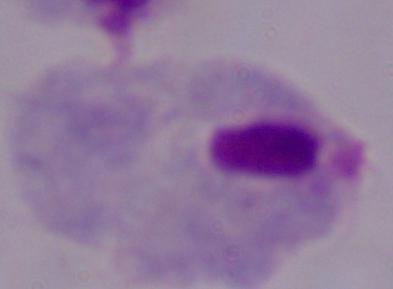 A trichomonad is seen. Photomicrograph. 1000x magnification.